Name the blood parasite species.
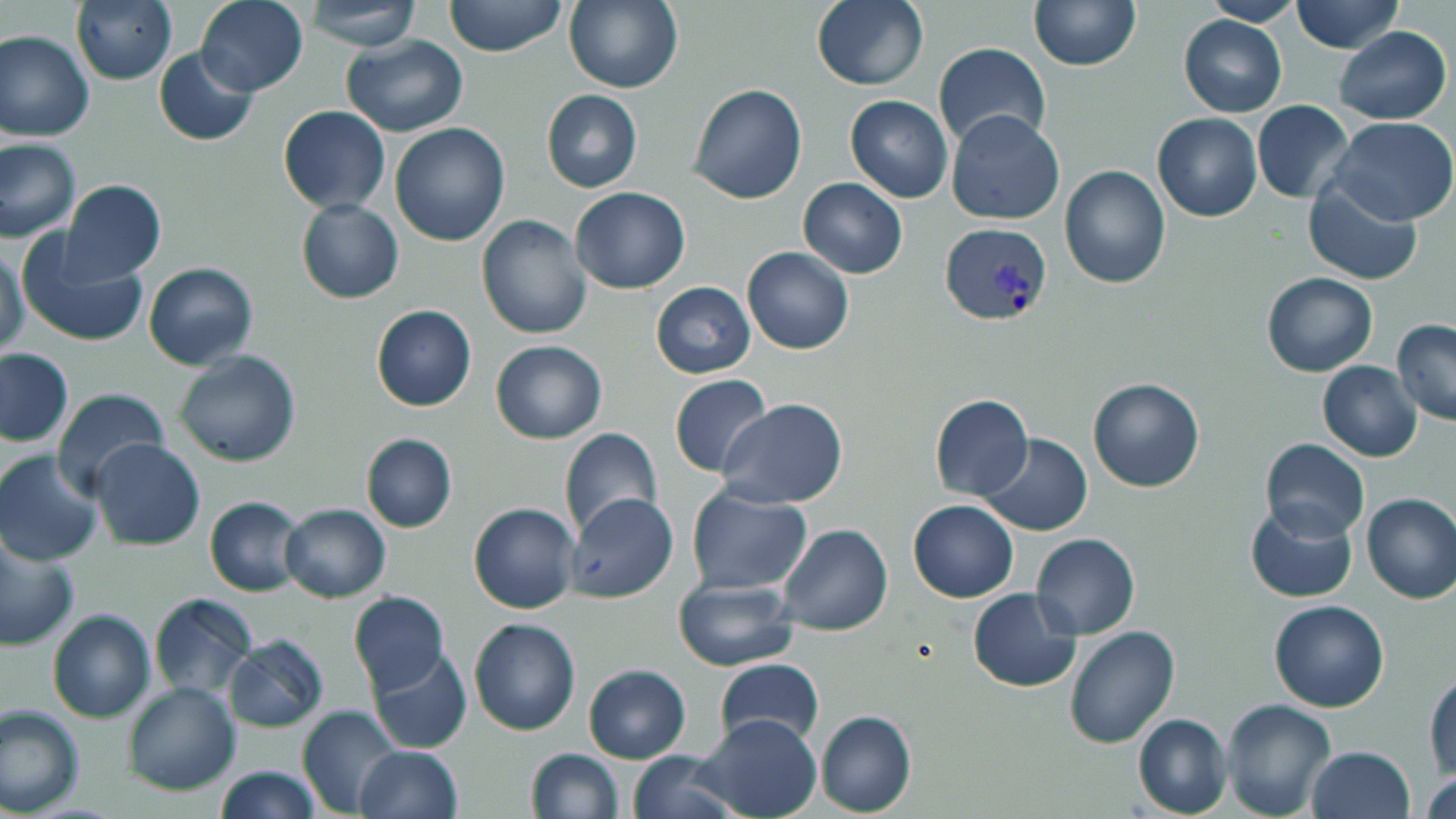

Plasmodium vivax.

Approximate bounding boxes as named x1/y1/x2/y2 corners in pixels. Uninfected red blood cell locations: (x1=195, y1=0, x2=309, y2=97), (x1=444, y1=0, x2=566, y2=57), (x1=810, y1=0, x2=928, y2=90), (x1=71, y1=1, x2=177, y2=84), (x1=306, y1=1, x2=421, y2=50), (x1=566, y1=1, x2=684, y2=94), (x1=1030, y1=1, x2=1141, y2=71), (x1=1200, y1=1, x2=1304, y2=26), (x1=1293, y1=1, x2=1401, y2=53), (x1=1179, y1=15, x2=1287, y2=117), (x1=1334, y1=26, x2=1451, y2=124), (x1=1, y1=30, x2=94, y2=143), (x1=341, y1=34, x2=470, y2=138), (x1=933, y1=43, x2=1051, y2=154), (x1=152, y1=47, x2=258, y2=146), (x1=688, y1=83, x2=808, y2=204), (x1=541, y1=90, x2=642, y2=192), (x1=845, y1=95, x2=953, y2=203), (x1=1252, y1=103, x2=1355, y2=202), (x1=278, y1=106, x2=391, y2=214), (x1=946, y1=111, x2=1065, y2=226), (x1=1152, y1=113, x2=1262, y2=222), (x1=1328, y1=117, x2=1456, y2=226), (x1=390, y1=122, x2=511, y2=247), (x1=0, y1=138, x2=80, y2=243), (x1=1060, y1=164, x2=1170, y2=289), (x1=799, y1=177, x2=907, y2=278), (x1=61, y1=179, x2=166, y2=283), (x1=1302, y1=182, x2=1422, y2=286), (x1=569, y1=188, x2=691, y2=293), (x1=295, y1=198, x2=404, y2=304), (x1=477, y1=216, x2=594, y2=339), (x1=16, y1=233, x2=151, y2=349), (x1=1, y1=246, x2=29, y2=358), (x1=741, y1=247, x2=854, y2=355), (x1=143, y1=261, x2=259, y2=370), (x1=1262, y1=273, x2=1378, y2=375), (x1=651, y1=282, x2=755, y2=378), (x1=370, y1=304, x2=476, y2=412), (x1=1391, y1=319, x2=1456, y2=426), (x1=490, y1=339, x2=607, y2=444), (x1=0, y1=347, x2=73, y2=447), (x1=173, y1=349, x2=302, y2=467), (x1=1317, y1=361, x2=1422, y2=461), (x1=669, y1=374, x2=772, y2=478), (x1=1087, y1=378, x2=1207, y2=493), (x1=51, y1=387, x2=169, y2=500), (x1=929, y1=393, x2=1034, y2=501), (x1=718, y1=398, x2=849, y2=509), (x1=559, y1=429, x2=663, y2=540), (x1=360, y1=432, x2=457, y2=533), (x1=978, y1=432, x2=1093, y2=536), (x1=1261, y1=438, x2=1369, y2=543), (x1=92, y1=440, x2=204, y2=551), (x1=1, y1=450, x2=102, y2=565), (x1=686, y1=487, x2=813, y2=595), (x1=1362, y1=492, x2=1456, y2=604), (x1=567, y1=493, x2=679, y2=605), (x1=205, y1=496, x2=306, y2=597), (x1=908, y1=500, x2=1018, y2=603), (x1=469, y1=502, x2=579, y2=614), (x1=1244, y1=502, x2=1359, y2=604), (x1=279, y1=503, x2=391, y2=602), (x1=776, y1=523, x2=891, y2=633), (x1=1030, y1=533, x2=1141, y2=640), (x1=0, y1=538, x2=79, y2=652), (x1=673, y1=580, x2=799, y2=671), (x1=967, y1=588, x2=1081, y2=694), (x1=348, y1=590, x2=451, y2=696), (x1=149, y1=593, x2=257, y2=698), (x1=1269, y1=601, x2=1390, y2=713), (x1=46, y1=609, x2=156, y2=724), (x1=468, y1=617, x2=581, y2=737), (x1=1064, y1=627, x2=1180, y2=748), (x1=223, y1=634, x2=329, y2=733), (x1=367, y1=648, x2=471, y2=753), (x1=715, y1=657, x2=824, y2=748), (x1=583, y1=664, x2=691, y2=763), (x1=1426, y1=670, x2=1456, y2=780), (x1=122, y1=681, x2=241, y2=797), (x1=1222, y1=700, x2=1335, y2=819), (x1=296, y1=704, x2=402, y2=816), (x1=0, y1=705, x2=84, y2=817), (x1=815, y1=709, x2=916, y2=817), (x1=692, y1=713, x2=822, y2=819), (x1=1133, y1=713, x2=1232, y2=817), (x1=354, y1=744, x2=464, y2=819), (x1=1306, y1=746, x2=1416, y2=819), (x1=525, y1=748, x2=623, y2=818), (x1=624, y1=750, x2=737, y2=819), (x1=214, y1=764, x2=320, y2=819), (x1=1422, y1=766, x2=1455, y2=819). Plasmodium vivax-infected red blood cell locations: (x1=939, y1=221, x2=1053, y2=326). Thin blood film. 1000x magnification. Light microscopy. One field of a larger specimen. Image is 1456×819 pixels. May-Grünwald-Giemsa-stained preparation.